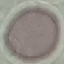

Summary:
  - Result: negative for malaria parasites
  - Stain: Giemsa
  - Image type: cell patch, automatically extracted from a larger field of view and resized to 64 × 64 pixels
  - Capture: smartphone camera at the microscope eyepiece
  - Preparation: thin blood smear